Describe the morphology of the red blood cells.
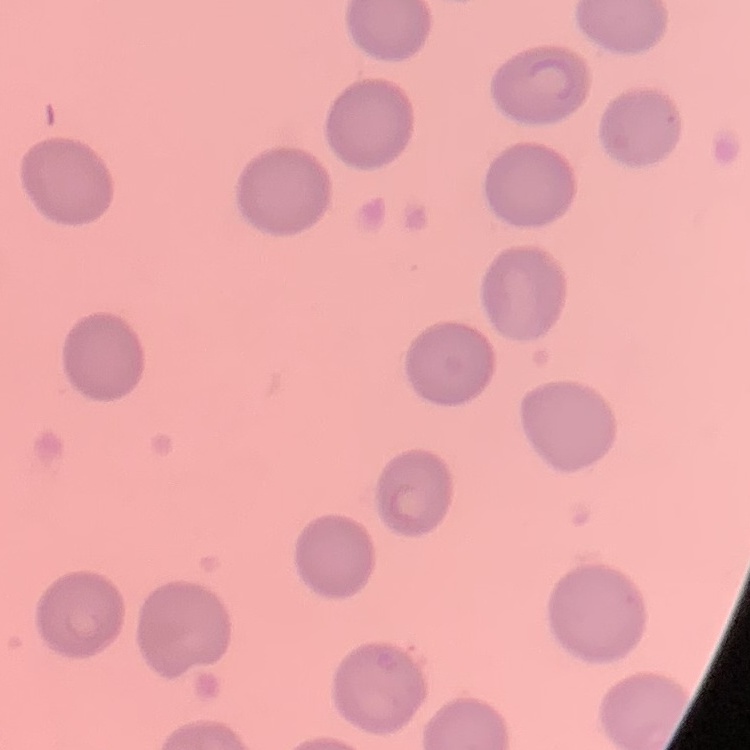

They show no rouleaux formation.

Thin peripheral smear. Stained with either Field's or Giemsa. Square crop of a larger photomicrograph.